Classify this cell by malaria status.
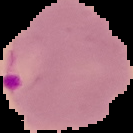

Parasitized.

The area outside the segmented cell region is set to black. From a thin blood smear. Image is 133×133 pixels.